Classify this cell by malaria status.
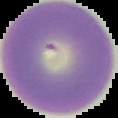

It is uninfected.

image type = cell region segmented out of the field of view; surrounding area masked to black
image size = 118×118 pixels
preparation = thin blood film